Identify the blood parasite species.
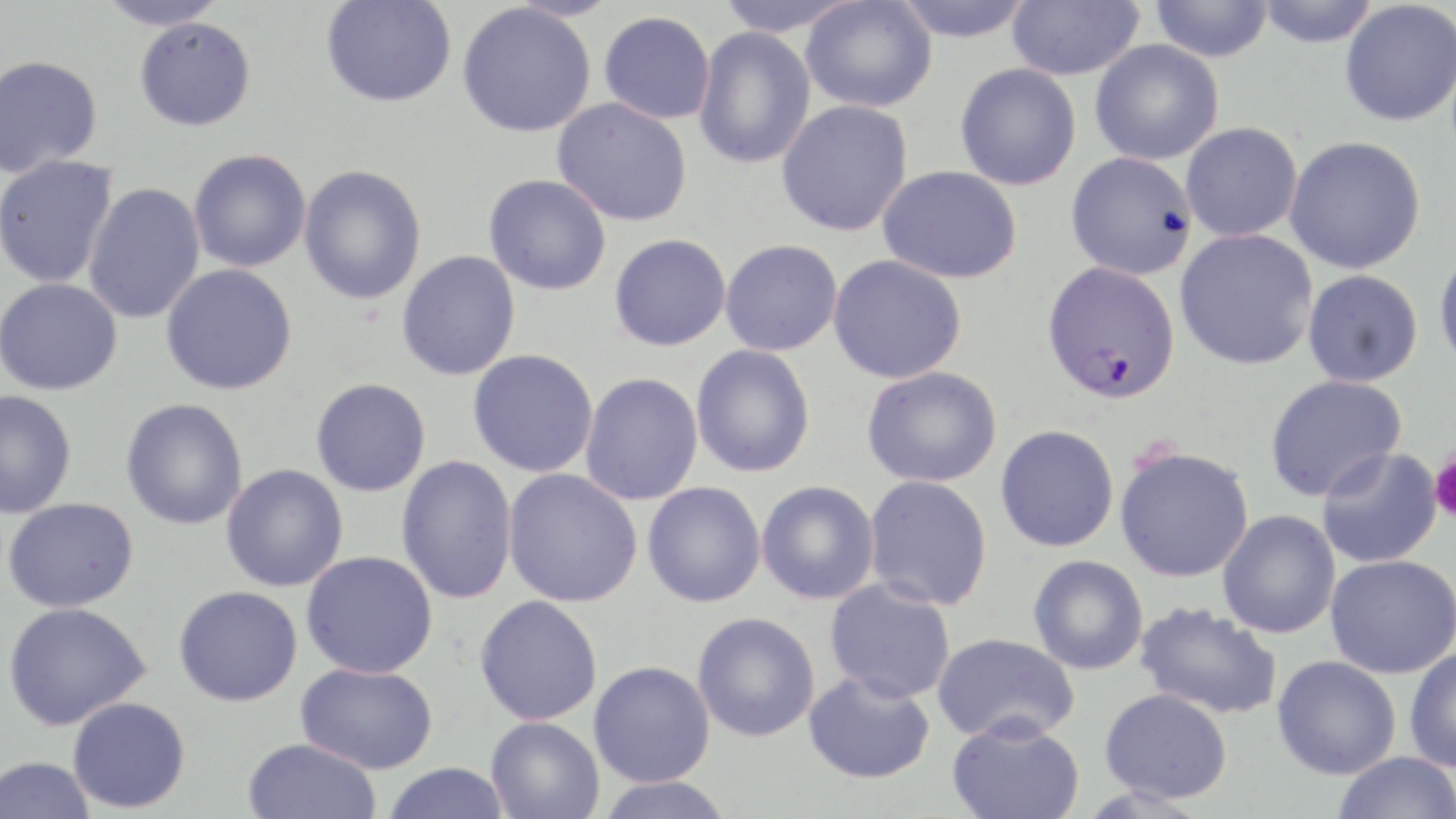

Plasmodium falciparum.

Summary:
  - Coordinate format: approximate bounding boxes as named x1/y1/x2/y2 corners in pixels
  - Uninfected red blood cell locations: (x1=97, y1=0, x2=228, y2=31), (x1=321, y1=0, x2=456, y2=107), (x1=712, y1=0, x2=861, y2=37), (x1=801, y1=0, x2=937, y2=113), (x1=891, y1=0, x2=1037, y2=43), (x1=1006, y1=0, x2=1145, y2=80), (x1=1149, y1=0, x2=1274, y2=63), (x1=1254, y1=0, x2=1381, y2=48), (x1=1339, y1=2, x2=1456, y2=127), (x1=457, y1=4, x2=596, y2=138), (x1=599, y1=11, x2=715, y2=125), (x1=133, y1=17, x2=256, y2=131), (x1=693, y1=26, x2=816, y2=170), (x1=1090, y1=40, x2=1224, y2=165), (x1=0, y1=54, x2=102, y2=178), (x1=955, y1=63, x2=1082, y2=191), (x1=552, y1=97, x2=693, y2=227), (x1=776, y1=99, x2=914, y2=237), (x1=1180, y1=122, x2=1303, y2=242), (x1=1285, y1=135, x2=1426, y2=274), (x1=188, y1=148, x2=311, y2=273), (x1=1065, y1=151, x2=1199, y2=280), (x1=0, y1=155, x2=119, y2=289), (x1=299, y1=164, x2=427, y2=305), (x1=878, y1=165, x2=1023, y2=284), (x1=483, y1=174, x2=611, y2=296), (x1=82, y1=182, x2=206, y2=324), (x1=1175, y1=229, x2=1319, y2=370), (x1=609, y1=233, x2=731, y2=351), (x1=720, y1=239, x2=843, y2=356), (x1=1433, y1=246, x2=1456, y2=377), (x1=397, y1=250, x2=521, y2=381), (x1=828, y1=254, x2=968, y2=383), (x1=160, y1=263, x2=298, y2=396), (x1=1302, y1=269, x2=1424, y2=387), (x1=0, y1=277, x2=123, y2=395), (x1=691, y1=344, x2=816, y2=478), (x1=468, y1=349, x2=600, y2=478), (x1=862, y1=366, x2=1002, y2=488), (x1=580, y1=372, x2=704, y2=506), (x1=1265, y1=374, x2=1408, y2=502), (x1=310, y1=378, x2=431, y2=497), (x1=0, y1=390, x2=77, y2=519), (x1=121, y1=398, x2=249, y2=530), (x1=995, y1=424, x2=1119, y2=552), (x1=1115, y1=446, x2=1254, y2=582), (x1=1316, y1=448, x2=1443, y2=569), (x1=396, y1=455, x2=518, y2=605), (x1=221, y1=463, x2=348, y2=592), (x1=503, y1=468, x2=642, y2=607), (x1=863, y1=474, x2=993, y2=611), (x1=756, y1=480, x2=880, y2=605), (x1=642, y1=481, x2=766, y2=608), (x1=2, y1=497, x2=139, y2=612), (x1=1218, y1=510, x2=1341, y2=638), (x1=300, y1=550, x2=438, y2=679), (x1=1324, y1=554, x2=1456, y2=678), (x1=1028, y1=555, x2=1149, y2=675), (x1=824, y1=578, x2=956, y2=703), (x1=174, y1=585, x2=303, y2=706), (x1=474, y1=594, x2=603, y2=725), (x1=3, y1=601, x2=150, y2=730), (x1=1135, y1=602, x2=1283, y2=720), (x1=692, y1=612, x2=821, y2=742), (x1=930, y1=632, x2=1080, y2=744), (x1=1404, y1=646, x2=1456, y2=772), (x1=1272, y1=655, x2=1401, y2=779), (x1=588, y1=660, x2=715, y2=788), (x1=296, y1=662, x2=438, y2=774), (x1=803, y1=670, x2=936, y2=785), (x1=1099, y1=687, x2=1233, y2=803), (x1=68, y1=696, x2=190, y2=813), (x1=486, y1=716, x2=604, y2=819), (x1=947, y1=717, x2=1084, y2=819), (x1=243, y1=738, x2=382, y2=819), (x1=1331, y1=751, x2=1455, y2=819), (x1=0, y1=755, x2=95, y2=818), (x1=381, y1=762, x2=511, y2=819), (x1=594, y1=775, x2=735, y2=819)
  - Platelet locations: (x1=1429, y1=450, x2=1456, y2=522)
  - Plasmodium falciparum-infected red blood cell locations: (x1=1042, y1=261, x2=1181, y2=405)
  - Image size: 1456×819 pixels
  - Field of view: one of a larger specimen
  - Preparation: thin blood film
  - Modality: light microscopy
  - Magnification: 1000x
  - Stain: May-Grünwald-Giemsa